Assess the morphology of the red blood cells.
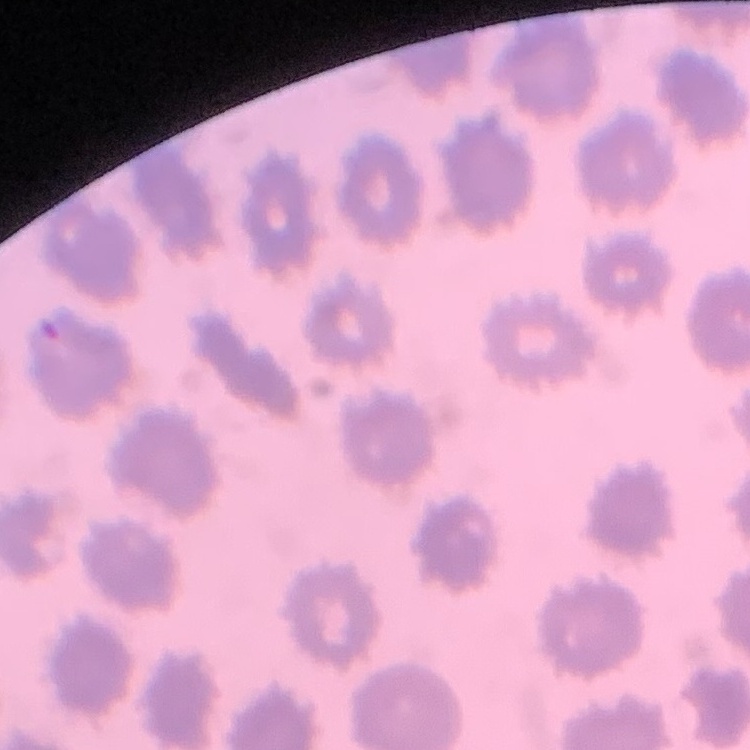
No rouleaux formation.

stain: Field's or Giemsa
image_type: one tile cut from a larger photomicrograph
preparation: thin blood smear